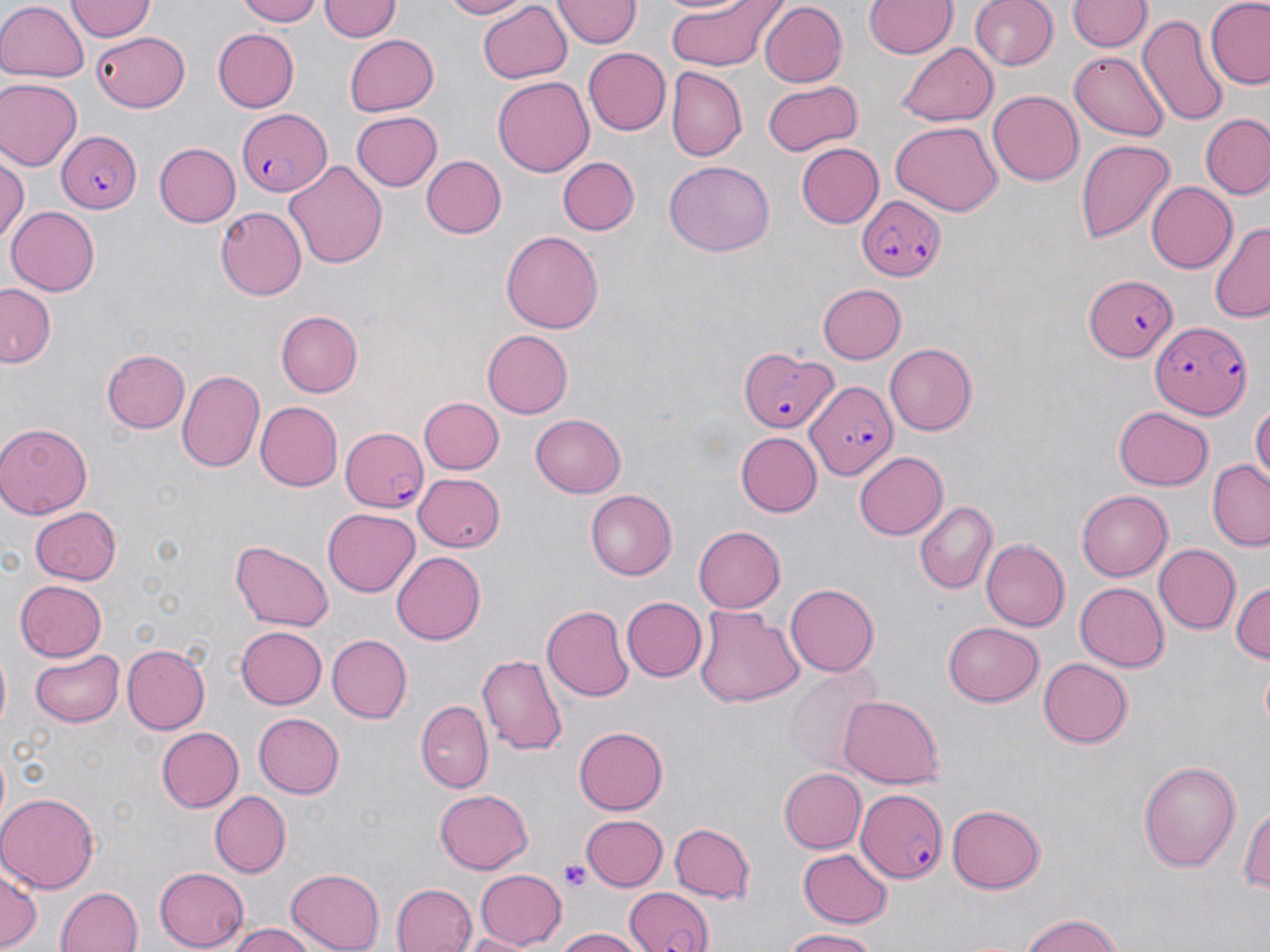
{
  "plasmodium_falciparum_infected_red_blood_cell_locations": "approximate bounding boxes as named x1/y1/x2/y2 corners in pixels: (x1=233, y1=110, x2=330, y2=196), (x1=56, y1=129, x2=140, y2=215), (x1=856, y1=195, x2=946, y2=283), (x1=1084, y1=274, x2=1180, y2=360), (x1=1149, y1=319, x2=1251, y2=418), (x1=739, y1=346, x2=835, y2=434), (x1=805, y1=378, x2=896, y2=481), (x1=343, y1=426, x2=430, y2=512), (x1=854, y1=790, x2=948, y2=881), (x1=623, y1=886, x2=715, y2=952)",
  "slide_level_diagnosis": "Plasmodium falciparum",
  "modality": "light microscopy",
  "uninfected_red_blood_cell_locations": "approximate bounding boxes as named x1/y1/x2/y2 corners in pixels: (x1=234, y1=0, x2=325, y2=25), (x1=436, y1=0, x2=532, y2=19), (x1=663, y1=0, x2=785, y2=72), (x1=864, y1=0, x2=956, y2=60), (x1=968, y1=0, x2=1057, y2=72), (x1=66, y1=1, x2=156, y2=42), (x1=318, y1=1, x2=401, y2=44), (x1=475, y1=1, x2=573, y2=84), (x1=554, y1=1, x2=638, y2=48), (x1=1067, y1=1, x2=1148, y2=53), (x1=1204, y1=1, x2=1270, y2=87), (x1=0, y1=3, x2=87, y2=83), (x1=752, y1=3, x2=940, y2=73), (x1=757, y1=3, x2=848, y2=88), (x1=1138, y1=11, x2=1230, y2=128), (x1=214, y1=27, x2=300, y2=112), (x1=90, y1=31, x2=190, y2=111), (x1=342, y1=34, x2=438, y2=117), (x1=899, y1=40, x2=998, y2=125), (x1=582, y1=46, x2=670, y2=135), (x1=1068, y1=50, x2=1170, y2=140), (x1=666, y1=69, x2=746, y2=163), (x1=492, y1=76, x2=594, y2=176), (x1=0, y1=79, x2=79, y2=171), (x1=761, y1=79, x2=861, y2=155), (x1=988, y1=90, x2=1084, y2=186), (x1=348, y1=111, x2=441, y2=192), (x1=1200, y1=113, x2=1270, y2=201), (x1=888, y1=121, x2=1002, y2=216), (x1=1076, y1=138, x2=1175, y2=244), (x1=152, y1=142, x2=240, y2=228), (x1=794, y1=143, x2=882, y2=228), (x1=423, y1=155, x2=505, y2=238), (x1=557, y1=156, x2=640, y2=236), (x1=0, y1=158, x2=27, y2=245), (x1=285, y1=159, x2=389, y2=269), (x1=662, y1=159, x2=775, y2=257), (x1=1147, y1=180, x2=1238, y2=273), (x1=6, y1=205, x2=101, y2=296), (x1=215, y1=207, x2=305, y2=300), (x1=1210, y1=222, x2=1270, y2=323), (x1=501, y1=230, x2=601, y2=336), (x1=818, y1=284, x2=907, y2=363), (x1=0, y1=285, x2=55, y2=367), (x1=275, y1=311, x2=362, y2=397), (x1=483, y1=329, x2=574, y2=418), (x1=883, y1=342, x2=976, y2=435), (x1=104, y1=348, x2=190, y2=434), (x1=177, y1=369, x2=266, y2=473), (x1=420, y1=396, x2=503, y2=475), (x1=1251, y1=399, x2=1270, y2=489), (x1=256, y1=401, x2=343, y2=490), (x1=1114, y1=407, x2=1214, y2=490), (x1=530, y1=414, x2=626, y2=497), (x1=0, y1=423, x2=94, y2=517), (x1=736, y1=433, x2=822, y2=517), (x1=854, y1=451, x2=948, y2=539), (x1=1208, y1=460, x2=1270, y2=550), (x1=413, y1=473, x2=505, y2=552), (x1=585, y1=489, x2=677, y2=580), (x1=1076, y1=490, x2=1173, y2=582), (x1=913, y1=500, x2=997, y2=594), (x1=29, y1=506, x2=120, y2=584), (x1=322, y1=508, x2=419, y2=596), (x1=692, y1=525, x2=784, y2=613), (x1=979, y1=539, x2=1069, y2=632), (x1=229, y1=542, x2=333, y2=631), (x1=1153, y1=544, x2=1240, y2=635), (x1=391, y1=551, x2=486, y2=645), (x1=1230, y1=579, x2=1270, y2=666), (x1=14, y1=580, x2=107, y2=660), (x1=1074, y1=582, x2=1168, y2=672), (x1=786, y1=584, x2=878, y2=676), (x1=622, y1=597, x2=707, y2=681), (x1=541, y1=605, x2=633, y2=701), (x1=694, y1=607, x2=803, y2=709), (x1=943, y1=621, x2=1044, y2=707), (x1=236, y1=626, x2=327, y2=709), (x1=327, y1=634, x2=412, y2=723), (x1=123, y1=644, x2=209, y2=732), (x1=31, y1=648, x2=124, y2=725), (x1=478, y1=652, x2=567, y2=756), (x1=1038, y1=657, x2=1134, y2=749), (x1=785, y1=663, x2=886, y2=776), (x1=839, y1=695, x2=944, y2=791), (x1=417, y1=700, x2=492, y2=792), (x1=253, y1=712, x2=345, y2=798), (x1=155, y1=725, x2=243, y2=812), (x1=576, y1=725, x2=670, y2=814), (x1=1139, y1=759, x2=1241, y2=873), (x1=779, y1=768, x2=866, y2=853), (x1=433, y1=788, x2=535, y2=874), (x1=208, y1=789, x2=290, y2=878), (x1=0, y1=791, x2=99, y2=893), (x1=1241, y1=801, x2=1270, y2=899), (x1=946, y1=803, x2=1045, y2=894), (x1=580, y1=814, x2=667, y2=891), (x1=668, y1=822, x2=754, y2=905), (x1=797, y1=847, x2=894, y2=929), (x1=155, y1=865, x2=249, y2=949), (x1=0, y1=866, x2=41, y2=951), (x1=474, y1=867, x2=566, y2=947), (x1=285, y1=868, x2=387, y2=951), (x1=391, y1=882, x2=479, y2=952), (x1=57, y1=886, x2=143, y2=952), (x1=1017, y1=913, x2=1129, y2=951), (x1=229, y1=924, x2=321, y2=952), (x1=550, y1=927, x2=648, y2=952), (x1=783, y1=929, x2=885, y2=951), (x1=459, y1=931, x2=534, y2=951)",
  "preparation": "thin blood smear",
  "platelet_locations": "approximate bounding boxes as named x1/y1/x2/y2 corners in pixels: (x1=558, y1=859, x2=591, y2=894)",
  "image_size": "1270×952 pixels",
  "magnification": "1000x",
  "field_of_view": "one of a larger specimen",
  "stain": "May-Grünwald-Giemsa"
}